Assess the morphology of the erythrocytes.
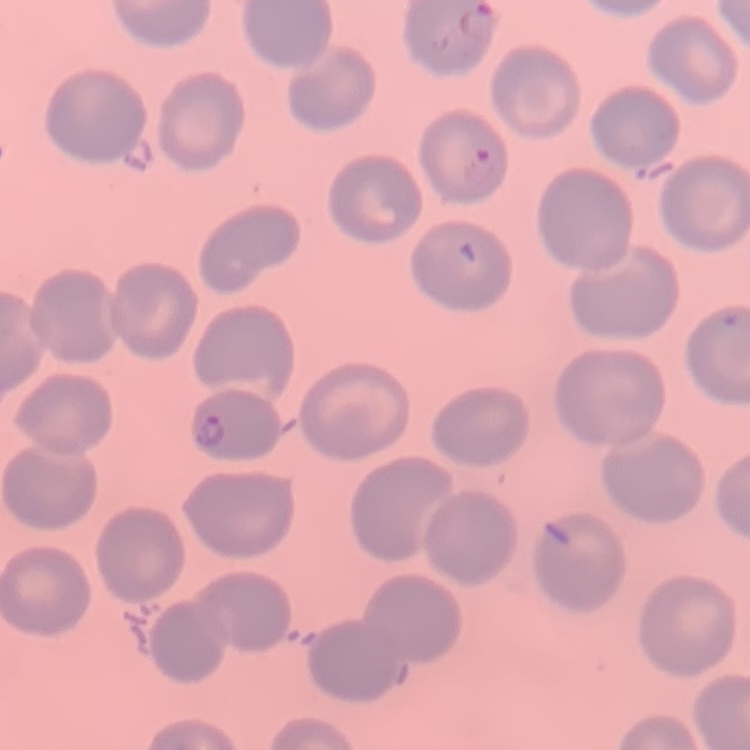

No rouleaux formation.

Stained with either Field's or Giemsa. Thin blood film. Square crop of a larger photomicrograph.